Classify this cell by malaria status.
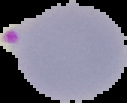
Parasitized.

image size = 127×103 pixels
preparation = thin blood film
image type = segmented cell region on a black background